Name the parasite shown.
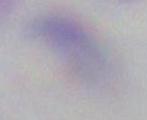
This is Toxoplasma gondii.

Summary:
  - Magnification: 1000x
  - Modality: micrograph